Evaluate for Plasmodium parasites.
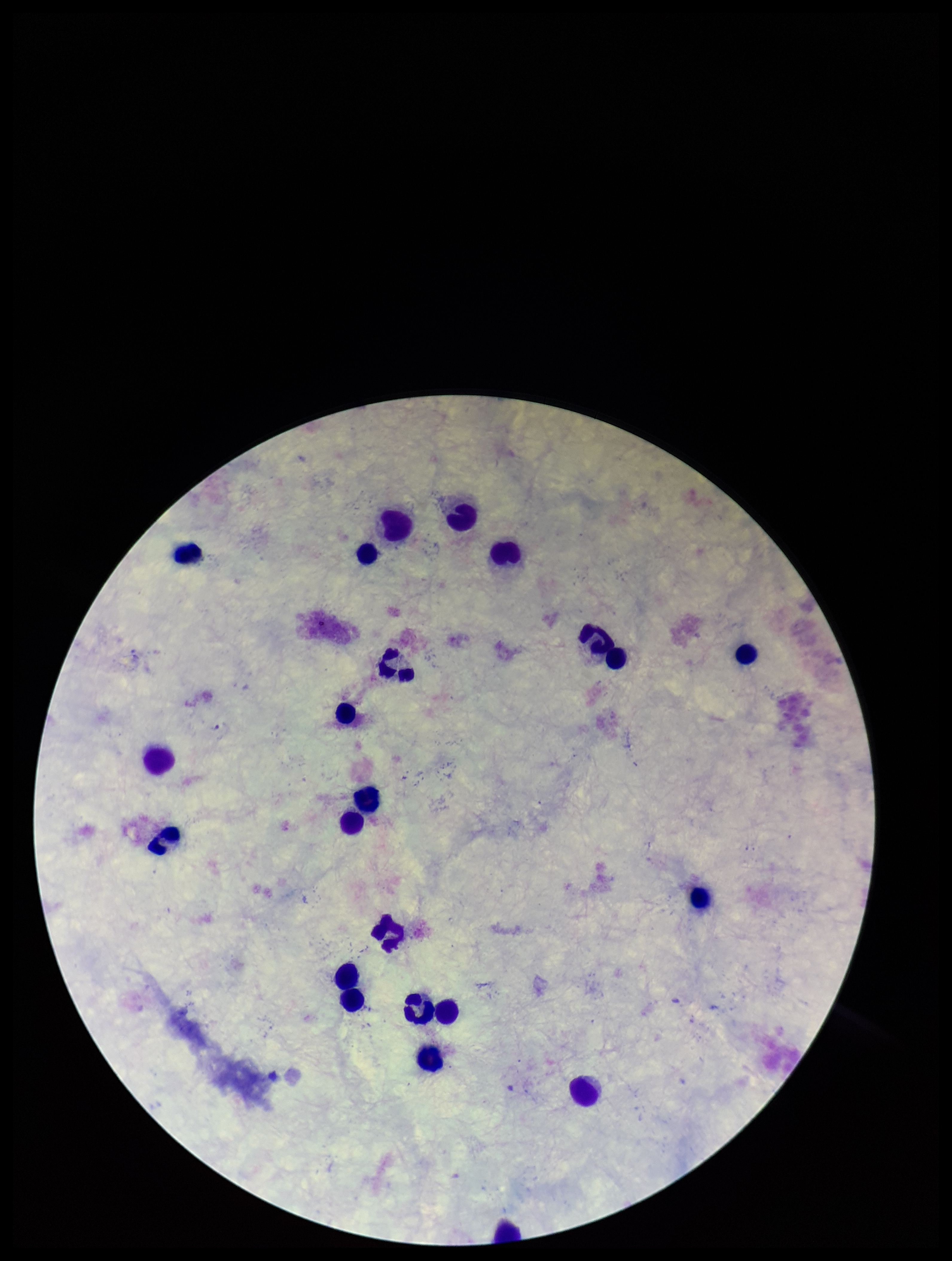

None identified.

Patient malaria status: negative. Photographed through the microscope eyepiece with a smartphone camera. Parasite count: 0. Image is 952×1261 pixels. Stained with Giemsa. Preparation: thick. Single field of view. Leukocyte count: 22.